Outline each Plasmodium falciparum-infected red blood cell.
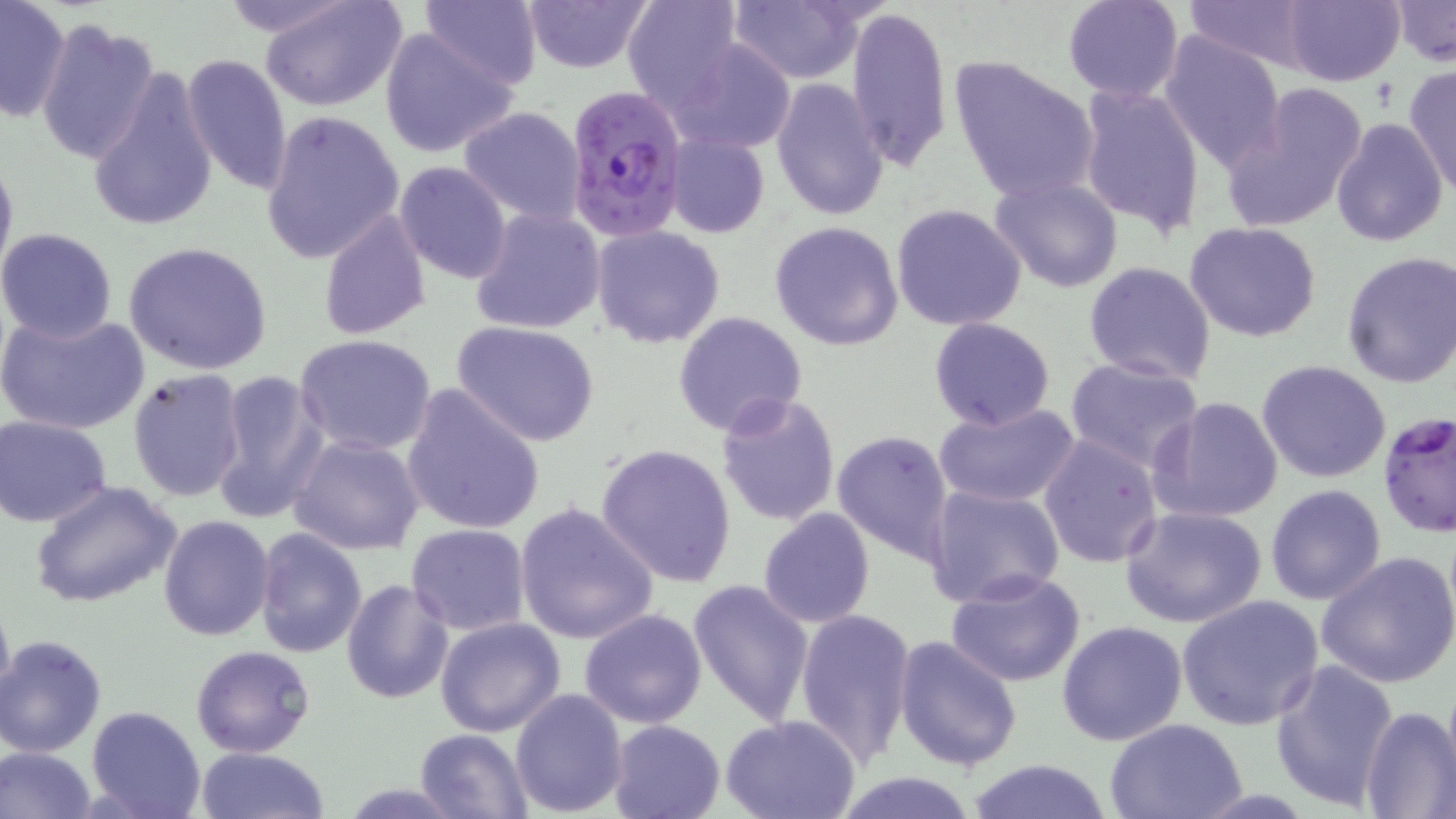

Approximate bounding boxes as (x1,y1)-(x2,y2) corner pairs in pixels.
Plasmodium falciparum-infected red blood cells (subset): (565,86)-(688,243).

Summary:
  - Uninfected red blood cell locations (subset): (214,0)-(366,44), (260,0)-(408,112), (419,0)-(545,89), (520,0)-(655,72), (623,0)-(742,115), (723,0)-(873,83), (1061,0)-(1185,103), (1182,0)-(1314,69), (1282,0)-(1403,87), (1390,1)-(1455,67), (0,2)-(71,121), (846,4)-(953,169), (34,17)-(160,164), (377,26)-(519,159), (1159,32)-(1285,172), (673,38)-(797,154), (180,54)-(292,198), (949,55)-(1100,204), (85,66)-(219,236), (1405,66)-(1456,194), (769,76)-(888,221), (1075,82)-(1205,239), (1226,85)-(1369,236), (458,106)-(585,225), (260,109)-(406,263), (1330,118)-(1449,247), (664,133)-(769,237), (0,146)-(17,287), (394,161)-(511,284), (991,176)-(1124,294), (890,203)-(1028,332), (469,207)-(606,335), (317,211)-(431,340), (770,221)-(904,351), (1184,221)-(1322,343), (592,226)-(725,349), (0,227)-(118,343), (123,241)-(273,375), (1340,250)-(1456,388), (1083,261)-(1216,386), (0,309)-(149,435), (673,310)-(807,438), (930,318)-(1055,431), (452,322)-(598,446), (294,334)-(437,456), (1064,356)-(1204,471), (1257,360)-(1391,483), (128,368)-(249,504), (211,370)-(328,524), (401,383)-(547,536), (715,390)-(840,527), (1150,396)-(1284,524), (934,402)-(1079,507), (2,416)-(115,528), (833,429)-(953,564), (1038,432)-(1163,569), (287,434)-(426,556), (596,441)-(738,587), (30,481)-(183,611), (923,484)-(1064,611), (1265,485)-(1385,604), (513,502)-(659,645), (1120,506)-(1267,629), (757,508)-(875,628), (157,514)-(274,642), (406,524)-(530,636), (254,527)-(367,658), (1316,548)-(1456,689), (944,570)-(1087,686), (341,578)-(454,704), (688,579)-(816,726), (0,590)-(15,714), (1176,595)-(1324,731), (578,608)-(707,730), (795,608)-(915,770), (434,616)-(566,737), (1056,621)-(1188,745), (893,635)-(1024,774), (1,636)-(105,757), (190,643)-(315,757), (1270,657)-(1399,812), (510,689)-(629,814), (1359,705)-(1455,817), (85,706)-(205,819), (720,715)-(861,819), (1104,718)-(1251,818), (607,719)-(727,819), (413,730)-(532,816), (195,746)-(330,819), (0,747)-(98,819), (964,758)-(1114,819), (828,770)-(986,819), (335,780)-(472,818)
  - Slide-level diagnosis: Plasmodium falciparum
  - Preparation: thin blood film
  - Magnification: 1000x
  - Modality: optical microscopy
  - Field of view: one of a larger specimen
  - Stain: May-Grünwald-Giemsa
  - Image size: 1456×819 pixels